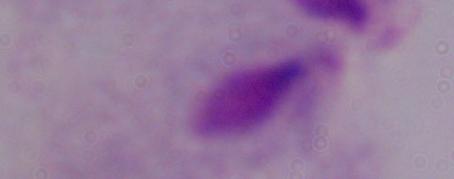
Captured at 1000x magnification. Micrograph. A trichomonad is shown.